Comment on the morphology of the erythrocytes.
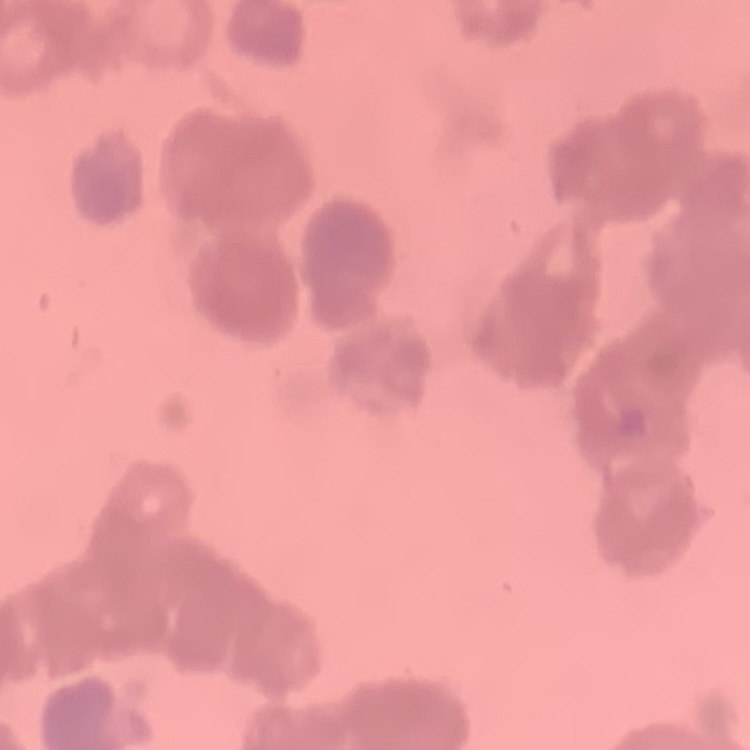
Rouleaux formation.

Summary:
  - Image type: square crop of a larger photomicrograph
  - Preparation: thin blood film
  - Stain: Field's or Giemsa